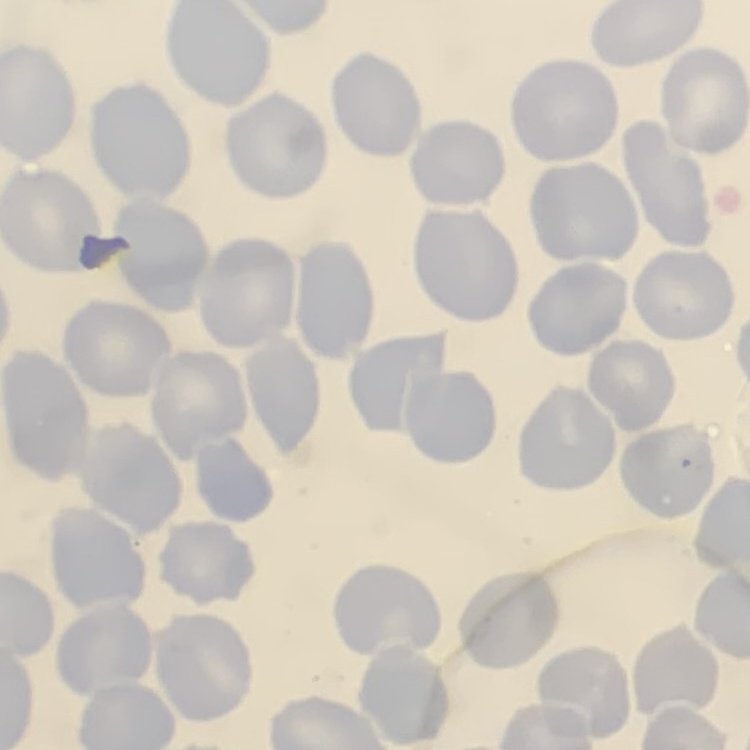

erythrocyte morphology = no rouleaux formation
image type = square crop of a larger photomicrograph
stain = Field's or Giemsa
preparation = thin blood film